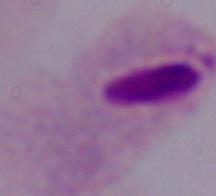

Micrograph. A trichomonad is shown. 1000x magnification.